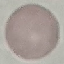

Malaria status: uninfected. Thin blood film. Cell patch, automatically extracted from a larger field of view and resized to 64 × 64 pixels. Giemsa stain. Acquired by smartphone through the microscope eyepiece.